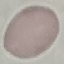 Malaria status: uninfected. Giemsa-stained preparation. Thin blood smear. Automatically extracted cell patch, resized to 64 × 64 pixels. Acquired by smartphone through the microscope eyepiece.